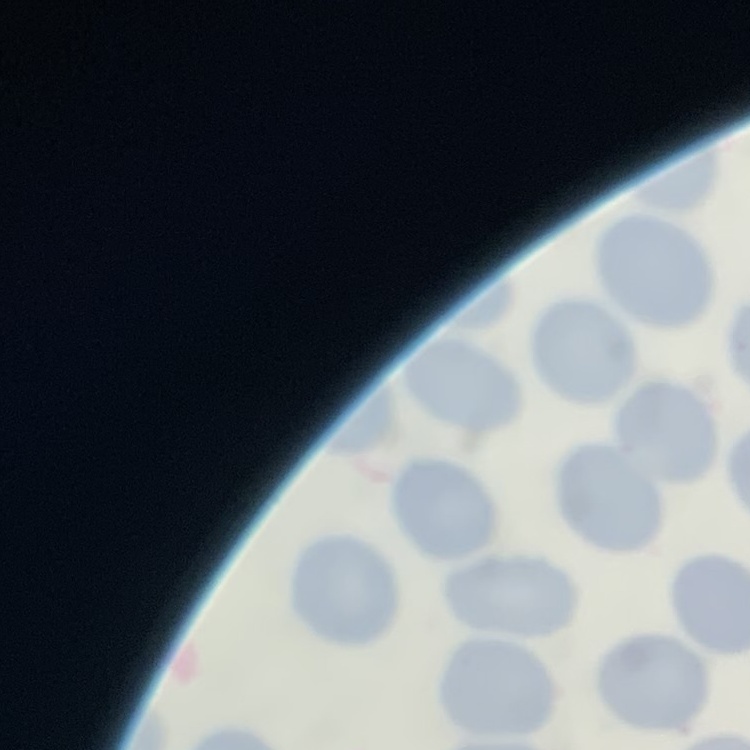
red blood cell morphology = no rouleaux formation
preparation = thin blood smear
image type = square crop of a larger photomicrograph
stain = Field's or Giemsa